Locate every blood parasite and identify its species.
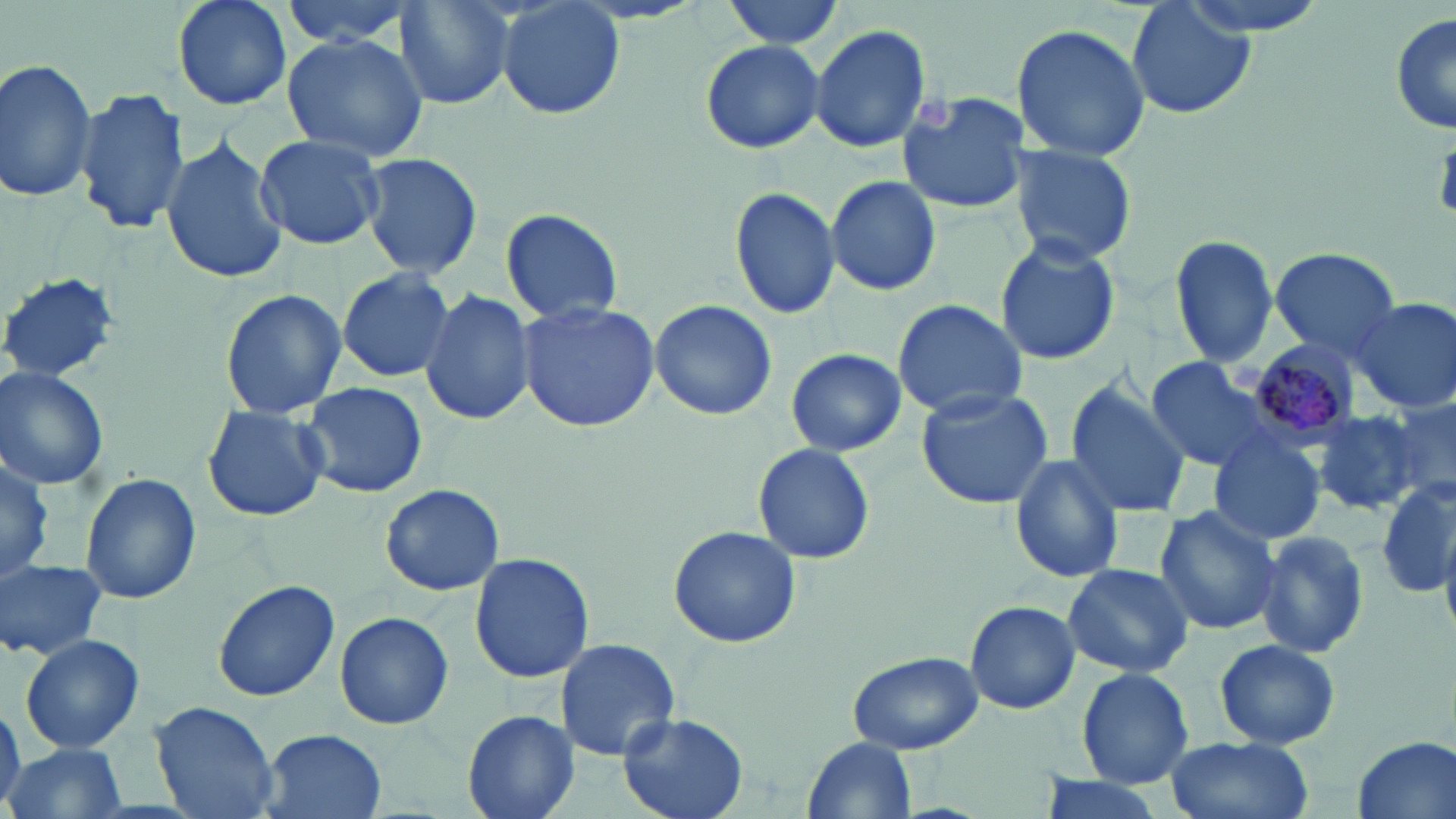

Approximate bounding boxes as [x1, y1, x2, y2] in pixels.
Plasmodium malariae-infected red blood cells: [1246, 338, 1362, 445].
No Plasmodium falciparum, Plasmodium ovale, Plasmodium vivax, Babesia divergens, or Trypanosoma brucei observed.

Summary:
  - Platelet locations: [915, 98, 957, 133]
  - Uninfected red blood cell locations: [172, 0, 291, 111], [278, 0, 421, 49], [392, 0, 518, 110], [495, 0, 626, 118], [720, 0, 845, 51], [1171, 0, 1336, 37], [1127, 1, 1257, 121], [1390, 14, 1455, 138], [1011, 22, 1150, 163], [808, 23, 932, 152], [282, 32, 428, 163], [700, 38, 825, 154], [0, 57, 100, 204], [74, 87, 189, 234], [896, 92, 1030, 214], [159, 133, 288, 287], [255, 133, 386, 249], [1012, 142, 1137, 266], [359, 150, 484, 283], [825, 174, 943, 297], [729, 186, 842, 322], [500, 207, 624, 324], [993, 234, 1120, 366], [1170, 234, 1279, 367], [1269, 247, 1401, 359], [336, 267, 454, 382], [0, 271, 124, 384], [221, 287, 344, 418], [421, 288, 536, 428], [1351, 295, 1455, 413], [891, 298, 1026, 421], [650, 299, 777, 421], [515, 301, 661, 431], [786, 348, 905, 458], [1142, 356, 1287, 474], [0, 367, 110, 490], [1064, 378, 1190, 521], [299, 381, 428, 499], [916, 387, 1055, 509], [1375, 393, 1456, 506], [201, 405, 331, 523], [1313, 407, 1431, 515], [1209, 436, 1325, 546], [753, 443, 876, 566], [0, 445, 52, 586], [1008, 453, 1126, 583], [80, 471, 201, 606], [1377, 479, 1452, 601], [380, 483, 506, 597], [1155, 504, 1282, 636], [667, 526, 803, 648], [1256, 530, 1371, 658], [468, 551, 595, 685], [0, 559, 108, 662], [1063, 563, 1194, 678], [212, 578, 340, 701], [965, 600, 1080, 713], [334, 610, 454, 730], [20, 634, 144, 754], [553, 637, 682, 762], [1212, 637, 1341, 749], [847, 651, 985, 756], [1077, 667, 1195, 788], [151, 699, 279, 819], [0, 703, 25, 814], [462, 708, 579, 819], [619, 712, 747, 819], [256, 728, 387, 819], [805, 735, 917, 816], [1166, 736, 1314, 819], [1350, 736, 1455, 819], [6, 742, 127, 819], [1034, 775, 1170, 819]
  - Slide-level diagnosis: Plasmodium malariae
  - Stain: May-Grünwald-Giemsa
  - Preparation: thin blood film
  - Modality: light microscopy
  - Magnification: 1000x
  - Field of view: single
  - Image size: 1456×819 pixels